Give the position of every leukocyte visible.
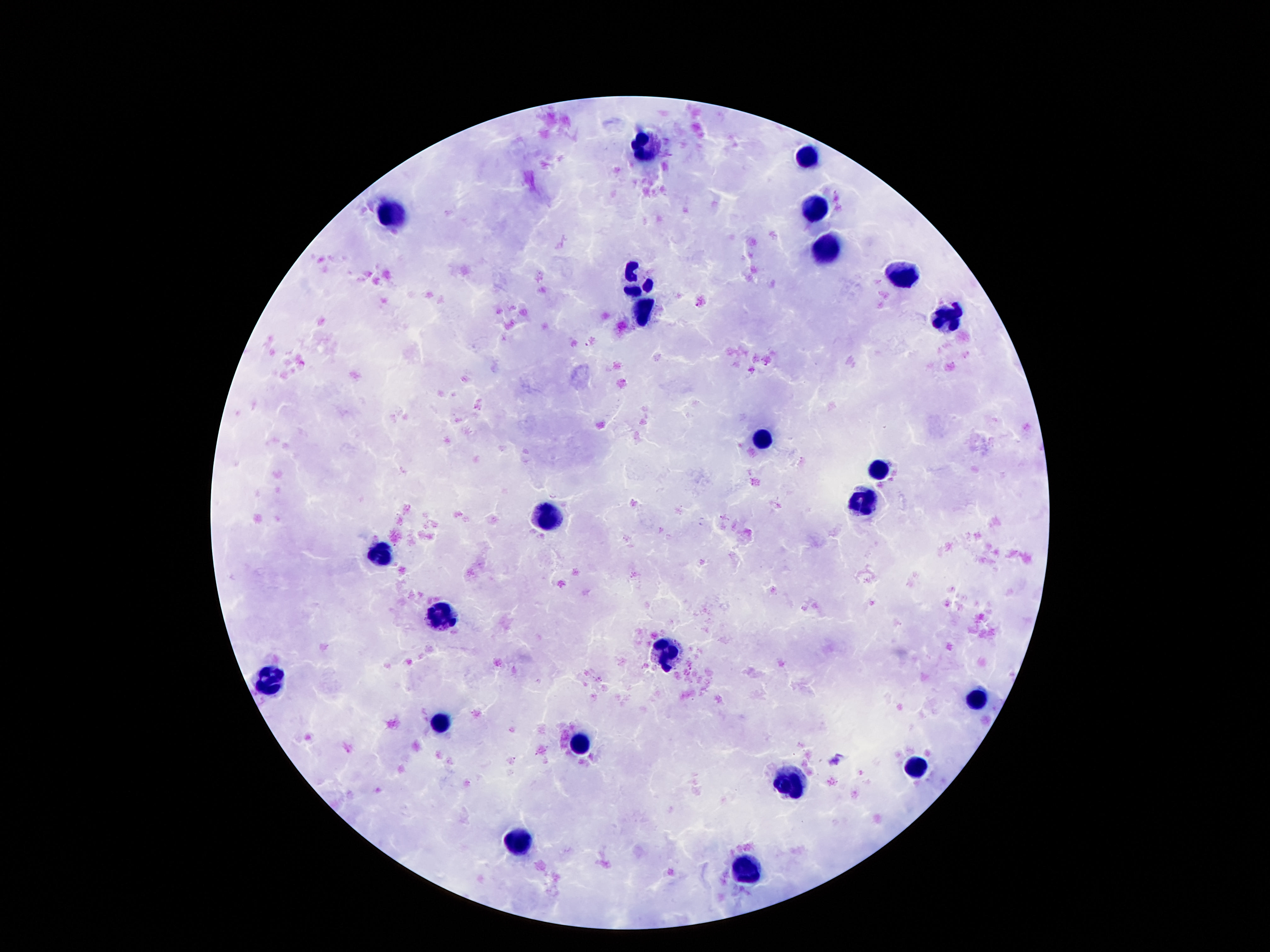
Approximate object centers, in pixels from the top-left corner.
Leukocytes: (x=648, y=142), (x=808, y=157), (x=814, y=211), (x=390, y=215), (x=825, y=250), (x=905, y=277), (x=638, y=280), (x=644, y=310), (x=948, y=320), (x=762, y=438), (x=879, y=467), (x=862, y=502), (x=553, y=515), (x=381, y=554), (x=437, y=613), (x=666, y=650), (x=274, y=680), (x=978, y=701), (x=441, y=723), (x=582, y=743), (x=915, y=766), (x=790, y=783), (x=523, y=841), (x=747, y=874).

Summary:
  - Stain: Giemsa
  - Magnification: 100x
  - Capture: smartphone camera through the microscope eyepiece
  - Image size: 1270×952 pixels
  - Preparation: thick blood smear
  - Patient malaria status: negative
  - Field of view: single